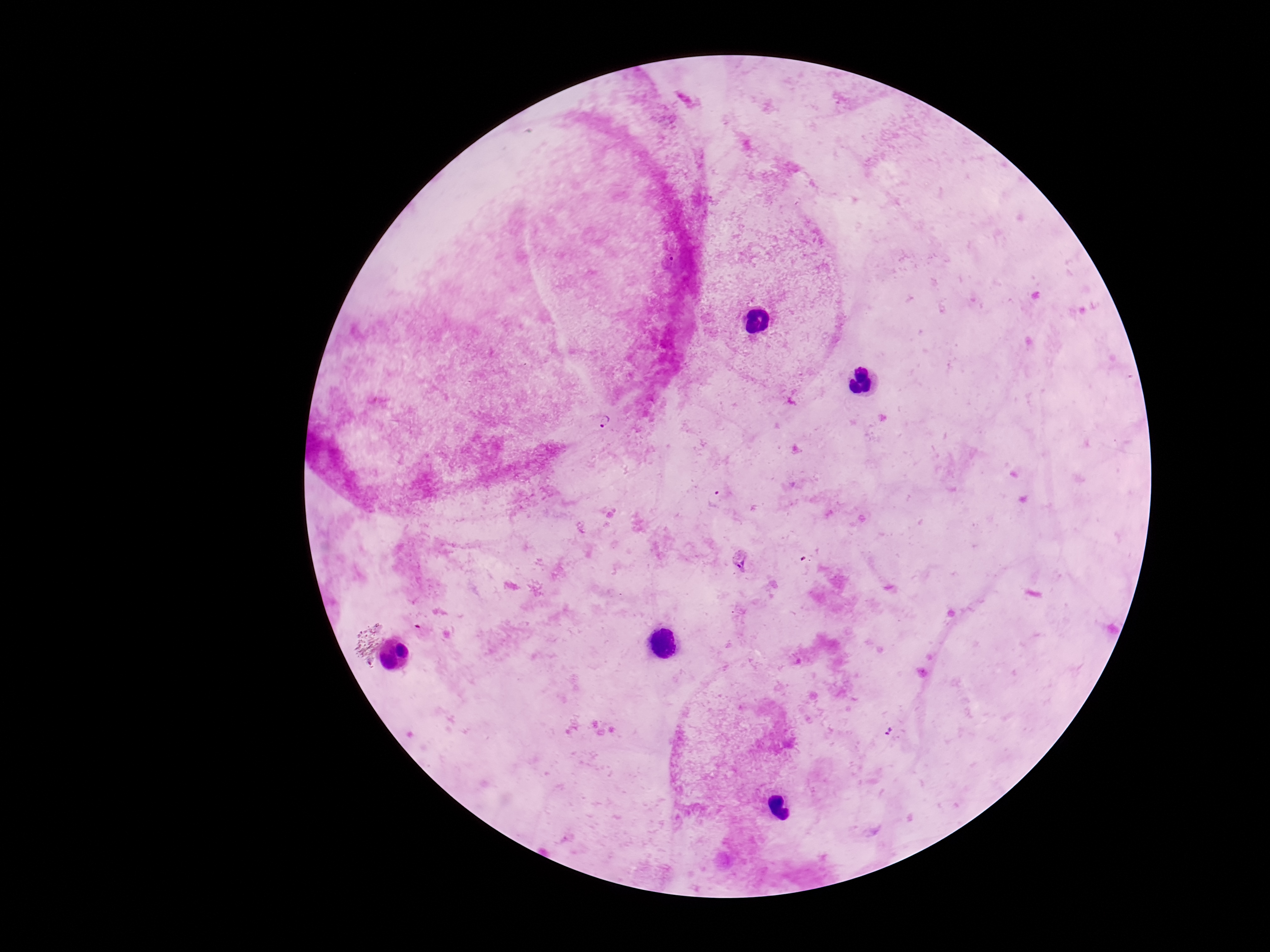
Approximate centers as {x, y} in pixels. Plasmodium parasite locations: {606, 421}, {713, 498}, {742, 564}. Giemsa stain. Patient malaria status: infected. Smartphone photograph taken through the microscope eyepiece. Image is 1270×952 pixels. Single field of view. 100x magnification. Thick blood smear.